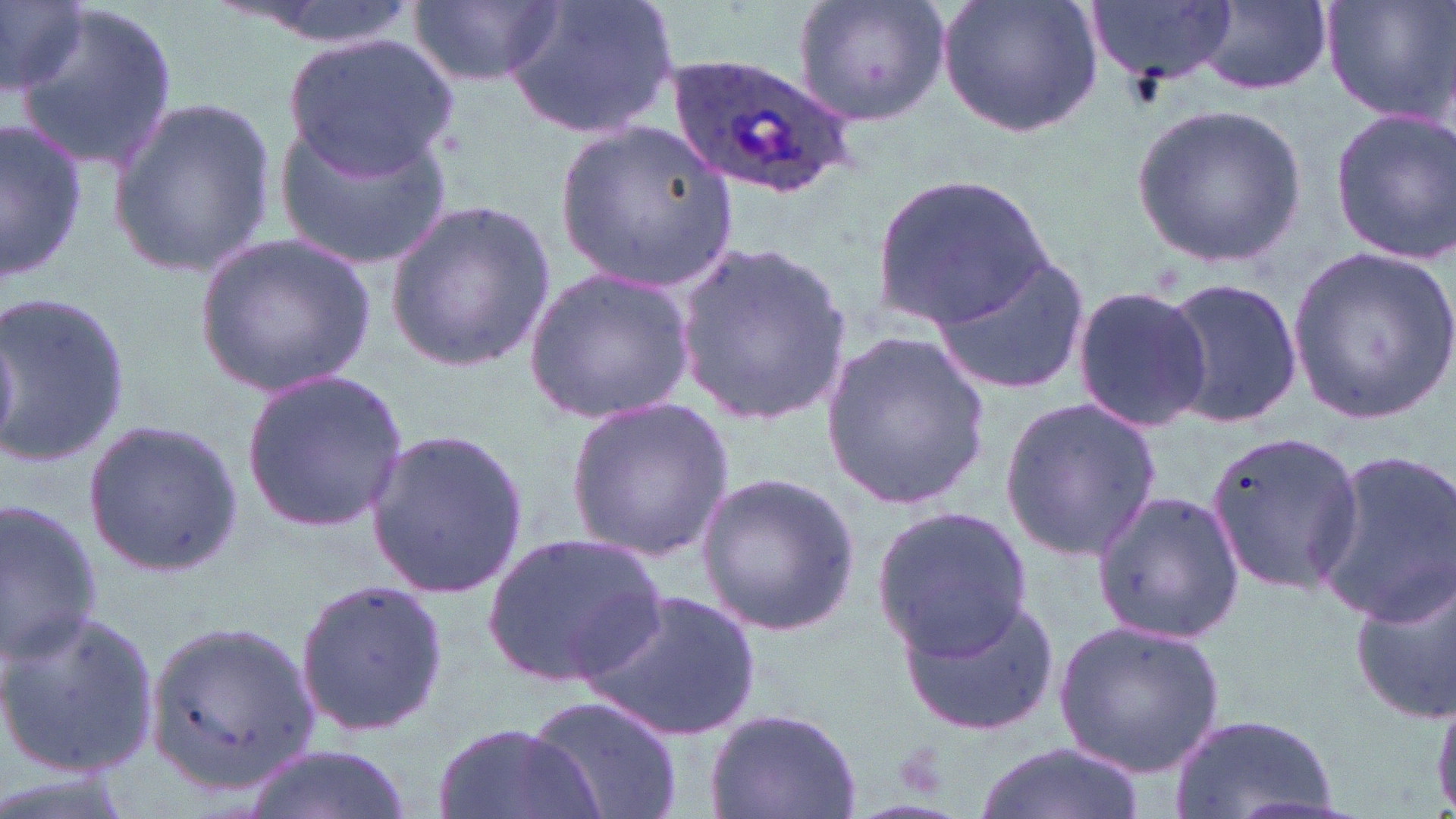

Approximate bounding boxes as [x1, y1, x2, y2] in pixels. Plasmodium ovale-infected red blood cell locations: [665, 53, 860, 201]. Uninfected red blood cell locations: [212, 0, 423, 50], [412, 0, 561, 90], [498, 0, 679, 140], [790, 0, 953, 130], [938, 0, 1102, 139], [1084, 0, 1238, 85], [1322, 0, 1456, 127], [1197, 1, 1333, 96], [0, 2, 93, 103], [15, 6, 177, 171], [285, 32, 457, 175], [108, 94, 276, 277], [1132, 100, 1308, 269], [1328, 110, 1456, 263], [276, 115, 455, 271], [1, 116, 89, 286], [558, 123, 737, 291], [873, 176, 1053, 326], [384, 198, 555, 374], [195, 230, 377, 399], [668, 236, 855, 426], [1287, 247, 1456, 422], [930, 250, 1090, 397], [524, 267, 696, 424], [1159, 276, 1302, 428], [1070, 285, 1213, 433], [0, 288, 131, 470], [819, 326, 990, 515], [240, 366, 410, 537], [998, 395, 1164, 560], [564, 396, 735, 559], [81, 418, 244, 575], [365, 428, 530, 597], [1200, 430, 1367, 595], [1310, 450, 1456, 629], [695, 469, 860, 636], [1090, 490, 1245, 643], [0, 498, 106, 664], [868, 502, 1037, 658], [482, 528, 671, 690], [1350, 570, 1456, 726], [294, 577, 448, 737], [586, 586, 761, 743], [895, 592, 1062, 737], [0, 609, 160, 777], [146, 616, 319, 792], [1053, 618, 1226, 776], [526, 694, 684, 819], [1431, 695, 1456, 818], [706, 704, 866, 819], [1168, 713, 1342, 819], [433, 719, 600, 819], [975, 740, 1143, 819], [243, 745, 413, 819]. Slide-level diagnosis: Plasmodium ovale. Thin blood film. Single field of view. Captured at 1000x magnification. Optical microscopy. Image is 1456×819 pixels. May-Grünwald-Giemsa stain.